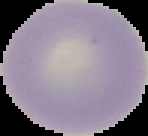
Summary:
  - Image type: segmented cell region on a black background
  - Malaria status: uninfected
  - Image size: 148×136 pixels
  - Preparation: thin blood film